Assess the morphology of the red blood cells.
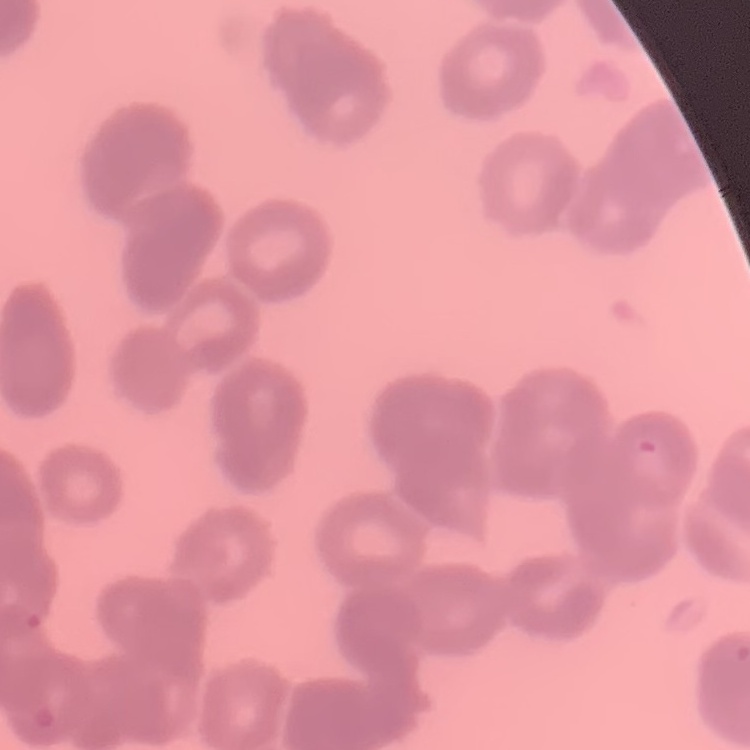

They show rouleaux formation.

Thin peripheral smear. One tile cut from a larger photomicrograph. Field's or Giemsa stain.